State which cell type is depicted.
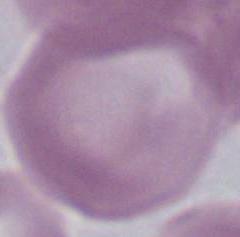

An erythrocyte.

{
  "modality": "photomicrograph",
  "magnification": "1000x"
}